Assess the morphology of the red blood cells.
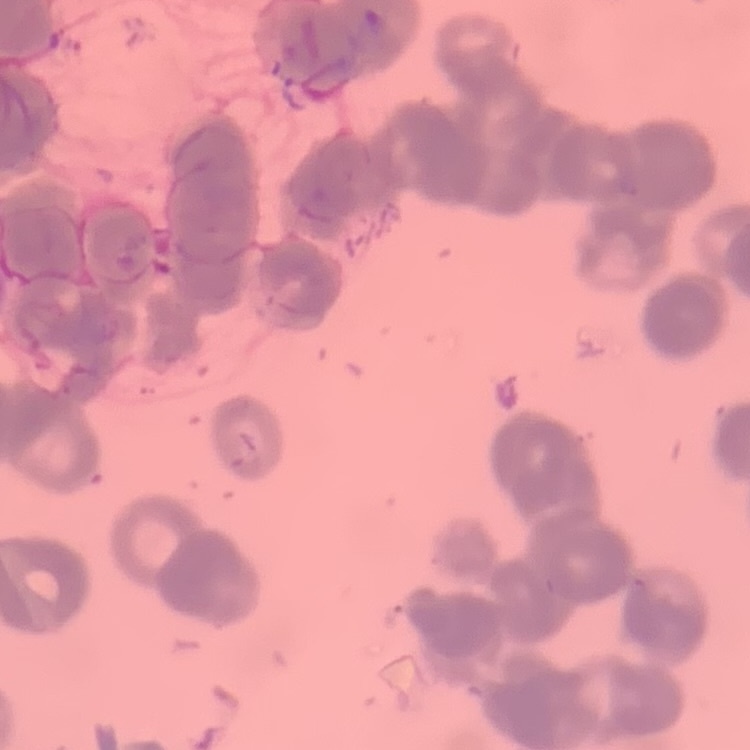

Rouleaux formation.

Stained with either Field's or Giemsa. Thin blood smear. One tile cut from a larger photomicrograph.